Assess the morphology of the red blood cells.
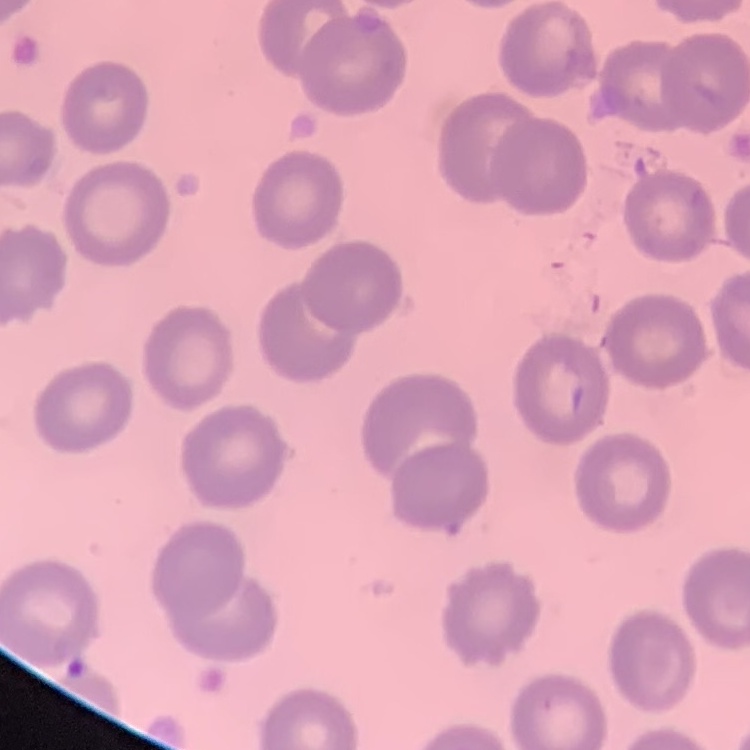
No rouleaux formation.

Field's or Giemsa stain. Thin blood film. Square crop of a larger photomicrograph.